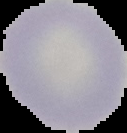

Summary:
  - Image size: 127×133 pixels
  - Image type: segmented cell region with the area outside set to black
  - Preparation: thin blood smear
  - Result: negative for malaria parasites